Report the malaria status of this cell.
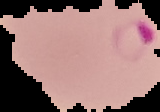
It is parasitized.

From a thin blood smear. The area outside the segmented cell region is set to black. Image is 160×112 pixels.